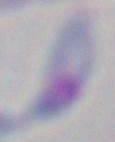

{
  "modality": "micrograph",
  "identification": "Toxoplasma gondii",
  "magnification": "1000x"
}